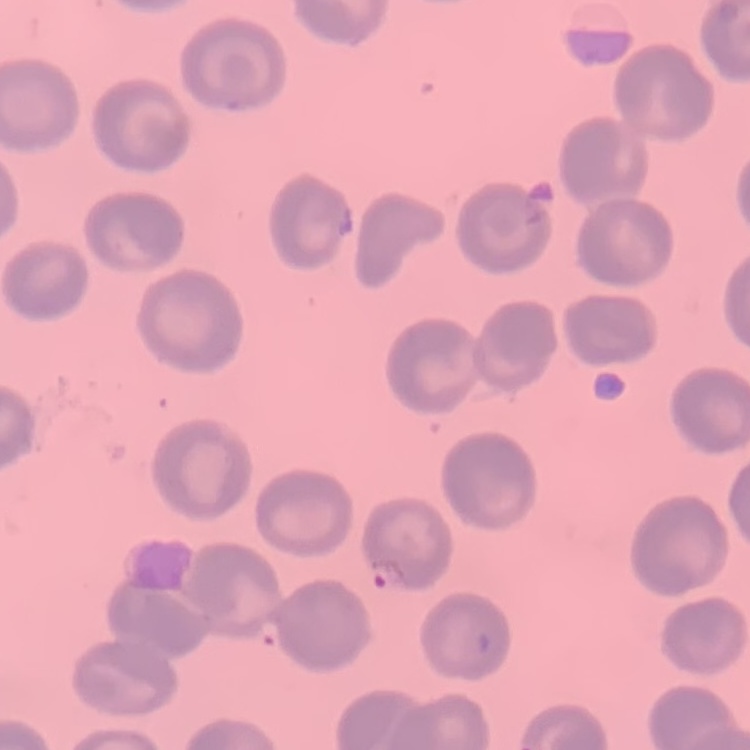
The red blood cells exhibit no rouleaux formation. One tile cut from a larger photomicrograph. Stained with either Field's or Giemsa. Thin blood smear.